Report the malaria status of this cell.
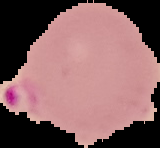

It is parasitized.

preparation = thin blood film
image size = 160×148 pixels
image type = segmented cell region with the area outside set to black